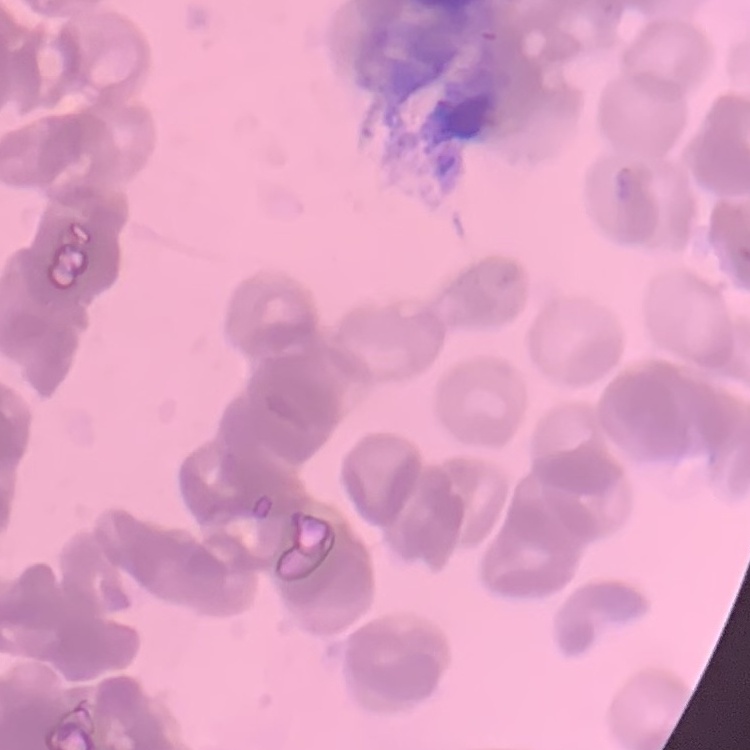

The erythrocytes show rouleaux formation. Field's or Giemsa stain. Thin peripheral smear. Square crop of a larger photomicrograph.